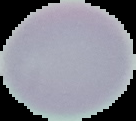
Image is 136×121 pixels. Malaria status: uninfected. From a thin blood smear. Segmented cell region on a black background.